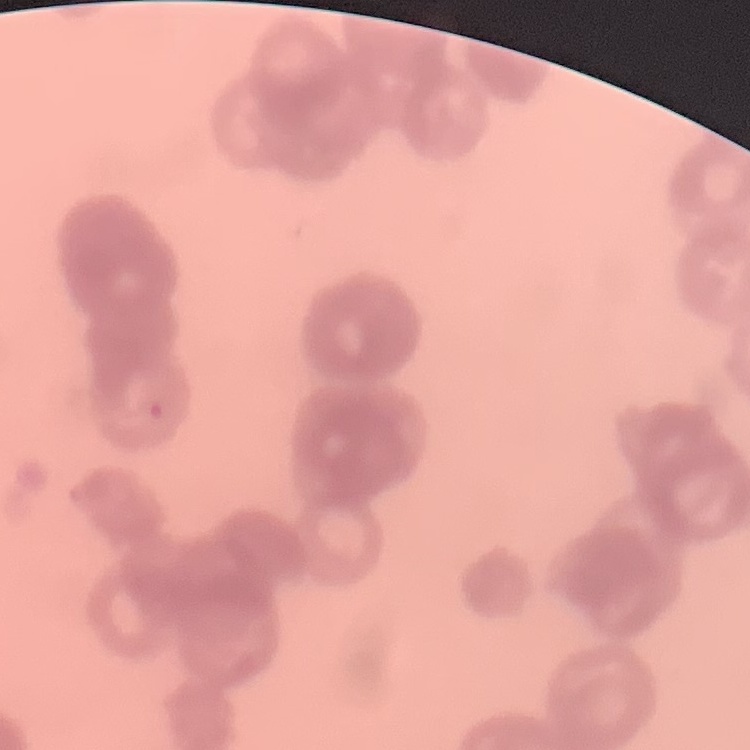
Summary:
  - Erythrocyte morphology: rouleaux formation
  - Preparation: thin peripheral smear
  - Image type: one tile cut from a larger photomicrograph
  - Stain: Field's or Giemsa